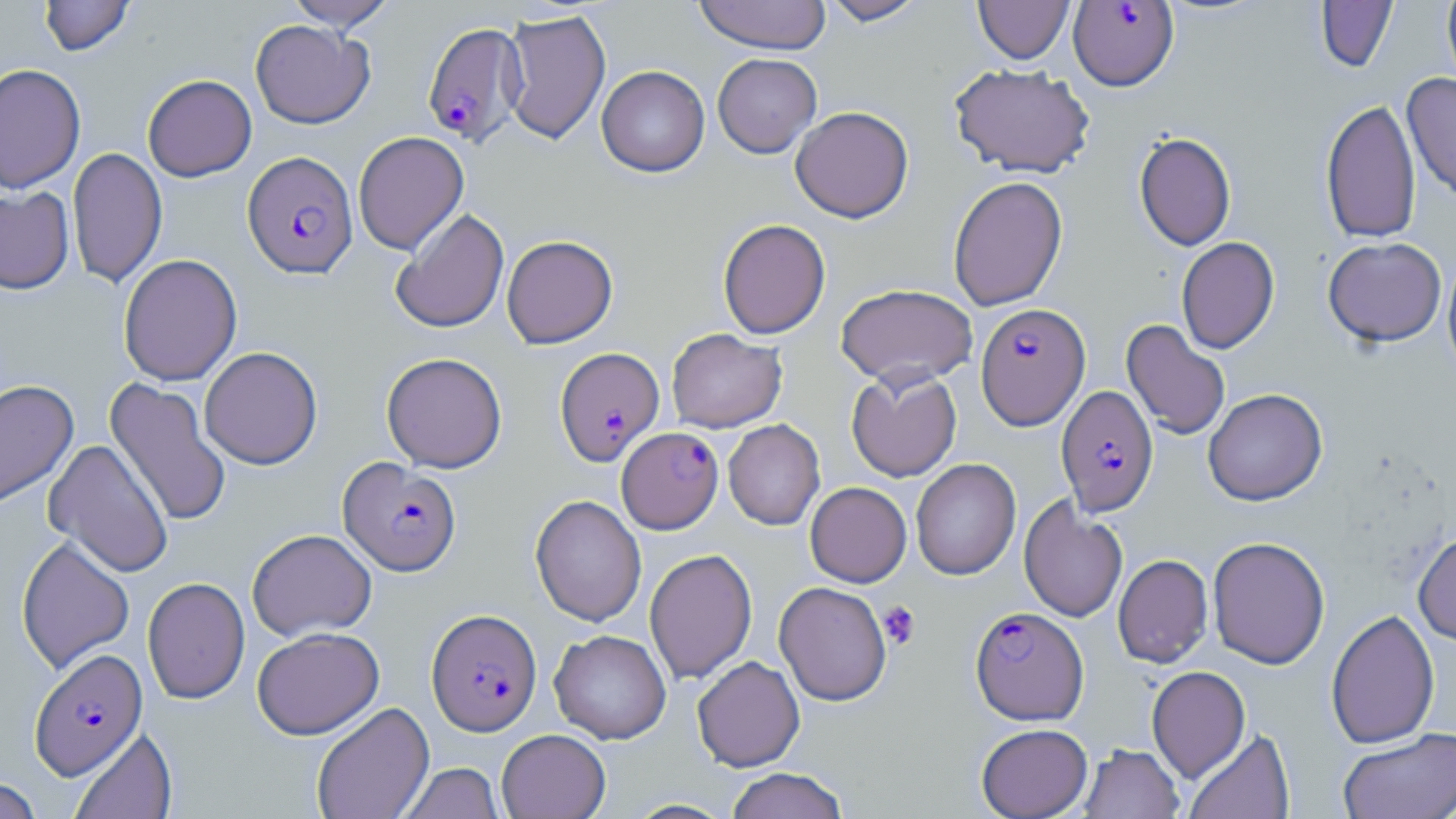

Approximate bounding boxes as (x1,y1)-(x2,y2) corner pairs in pixels. Uninfected red blood cell locations: (39,0)-(135,56), (284,0)-(398,32), (693,0)-(831,54), (819,0)-(929,25), (973,0)-(1074,64), (1441,0)-(1456,90), (1315,1)-(1398,73), (501,9)-(611,145), (250,19)-(374,129), (712,53)-(822,158), (949,62)-(1096,178), (0,63)-(86,194), (596,65)-(710,177), (1401,72)-(1456,204), (142,74)-(257,181), (1320,97)-(1421,244), (790,106)-(913,223), (353,131)-(469,255), (1134,131)-(1236,251), (67,146)-(167,289), (948,175)-(1068,311), (0,186)-(75,294), (391,208)-(510,333), (717,218)-(831,339), (502,235)-(618,348), (1176,237)-(1279,354), (1322,237)-(1446,347), (1442,252)-(1456,384), (118,254)-(242,386), (835,283)-(977,387), (1121,319)-(1231,440), (666,328)-(787,433), (199,346)-(323,469), (381,352)-(507,473), (846,366)-(962,482), (104,378)-(231,527), (0,379)-(79,509), (1203,388)-(1327,506), (723,419)-(825,530), (44,439)-(174,578), (911,458)-(1021,580), (805,482)-(911,587), (530,494)-(647,626), (1019,496)-(1128,622), (247,528)-(377,641), (1413,528)-(1456,645), (16,535)-(135,674), (1207,536)-(1330,669), (644,547)-(758,685), (1113,554)-(1213,668), (142,577)-(250,704), (773,581)-(892,705), (1326,608)-(1440,749), (252,626)-(384,739), (549,629)-(671,744), (692,655)-(805,772), (1147,665)-(1250,782), (311,702)-(434,819), (976,723)-(1092,819), (69,725)-(177,819), (1185,727)-(1295,819), (497,728)-(611,819), (1337,728)-(1456,819), (1079,743)-(1185,819), (398,762)-(504,819), (724,768)-(850,819), (1,777)-(44,818), (626,799)-(735,818). Plasmodium falciparum-infected red blood cell locations: (1069,1)-(1178,91), (423,21)-(528,147), (242,150)-(358,279), (976,303)-(1090,429), (554,347)-(665,465), (1056,385)-(1158,516), (617,427)-(723,533), (338,457)-(461,576), (968,606)-(1085,724), (426,608)-(541,736), (28,648)-(147,780). Platelet locations: (878,601)-(921,649). Slide-level diagnosis: Plasmodium falciparum. Image is 1456×819 pixels. Thin blood film. May-Grünwald-Giemsa stain. Light microscopy. 1000x magnification. One field of a larger specimen.